Assess this cell for malaria.
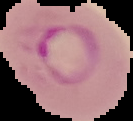

It is parasitized.

Summary:
  - Image type: segmented cell region with the area outside set to black
  - Image size: 133×121 pixels
  - Preparation: thin blood film